Locate platelets.
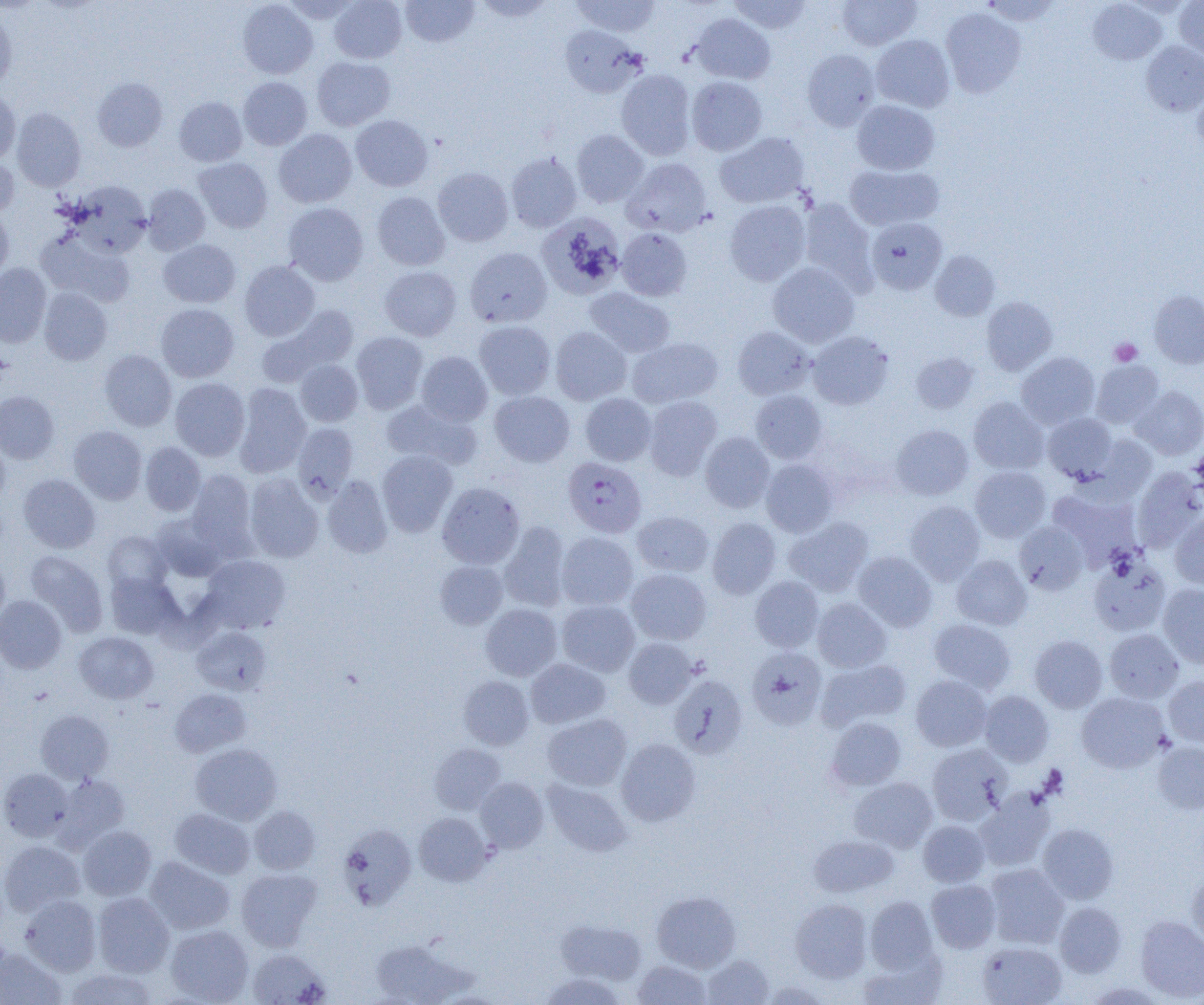

Approximate bounding boxes as [x1, y1, x2, y2] in pixels.
Platelets: [1109, 338, 1142, 365].

slide_level_diagnosis: Plasmodium falciparum
magnification: 1000x
plasmodium_falciparum_infected_red_blood_cell_locations: 'approximate bounding boxes as [x1, y1, x2, y2] in pixels: [563, 457, 646, 538]'
field_of_view: single
image_size: 1204×1005 pixels
modality: optical microscopy
preparation: thin blood film
uninfected_red_blood_cell_locations: 'approximate bounding boxes as [x1, y1, x2, y2] in pixels: [281, 0, 361, 23], [329, 0, 407, 63], [401, 0, 479, 47], [472, 0, 557, 22], [570, 0, 661, 37], [728, 0, 812, 34], [837, 0, 921, 50], [980, 0, 1062, 26], [1175, 0, 1204, 61], [238, 1, 317, 79], [1088, 1, 1166, 65], [0, 8, 17, 91], [941, 8, 1026, 98], [691, 14, 775, 84], [560, 25, 642, 97], [871, 35, 955, 112], [1141, 41, 1204, 115], [802, 49, 880, 131], [312, 56, 395, 130], [616, 69, 696, 159], [686, 76, 767, 156], [92, 77, 168, 151], [238, 77, 312, 150], [1193, 84, 1204, 155], [0, 92, 21, 164], [174, 97, 247, 166], [852, 99, 940, 175], [12, 107, 86, 192], [350, 115, 433, 191], [274, 129, 357, 208], [572, 130, 649, 207], [715, 132, 810, 208], [506, 151, 582, 232], [0, 154, 19, 219], [193, 157, 272, 233], [622, 158, 712, 237], [844, 164, 944, 232], [433, 167, 513, 246], [70, 181, 151, 256], [143, 184, 210, 255], [372, 192, 450, 270], [798, 198, 877, 293], [724, 200, 811, 286], [283, 203, 368, 285], [0, 207, 14, 281], [536, 212, 625, 299], [867, 217, 947, 295], [617, 228, 692, 301], [36, 230, 135, 308], [158, 239, 240, 308], [465, 247, 552, 328], [930, 250, 1000, 321], [239, 260, 320, 341], [768, 262, 859, 348], [0, 264, 51, 347], [380, 266, 462, 341], [39, 287, 112, 365], [585, 287, 675, 358], [1149, 290, 1204, 369], [981, 297, 1057, 376], [155, 304, 239, 382], [258, 305, 358, 386], [474, 320, 556, 400], [733, 326, 814, 399], [550, 327, 632, 405], [808, 331, 894, 409], [351, 332, 428, 414], [627, 337, 724, 408], [99, 350, 177, 430], [416, 351, 492, 426], [911, 352, 980, 414], [1016, 352, 1100, 429], [295, 359, 363, 427], [1091, 360, 1165, 428], [170, 378, 250, 460], [233, 383, 311, 478], [1132, 386, 1204, 459], [750, 390, 827, 463], [0, 391, 59, 463], [489, 391, 575, 467], [580, 393, 656, 466], [644, 396, 722, 480], [968, 397, 1049, 474], [380, 398, 481, 470], [1042, 413, 1117, 482], [293, 423, 358, 500], [891, 424, 973, 500], [69, 426, 147, 504], [700, 432, 774, 512], [0, 436, 10, 506], [1088, 436, 1157, 502], [140, 441, 205, 516], [377, 450, 457, 536], [760, 459, 839, 537], [970, 466, 1051, 542], [1132, 468, 1204, 551], [186, 469, 257, 554], [18, 473, 100, 552], [245, 473, 323, 563], [322, 475, 392, 558], [437, 482, 525, 569], [1047, 487, 1141, 570], [905, 501, 985, 584], [633, 511, 714, 576], [152, 513, 227, 581], [1170, 513, 1204, 589], [784, 516, 873, 596], [707, 517, 780, 599], [499, 521, 571, 612], [1014, 522, 1088, 595], [103, 531, 171, 594], [556, 532, 638, 610], [25, 550, 108, 637], [853, 551, 937, 632], [0, 552, 10, 628], [201, 555, 291, 632], [951, 555, 1032, 630], [1088, 557, 1171, 636], [435, 561, 508, 629], [626, 568, 711, 645], [106, 572, 182, 639], [750, 576, 824, 652], [1158, 584, 1204, 668], [0, 595, 67, 674], [812, 598, 892, 672], [557, 600, 640, 676], [481, 604, 562, 681], [929, 618, 1016, 694], [191, 626, 271, 694], [1104, 629, 1183, 703], [75, 632, 158, 703], [1029, 635, 1108, 713], [623, 637, 698, 708], [747, 647, 827, 730], [526, 658, 610, 728], [817, 659, 911, 732], [668, 674, 748, 759], [458, 675, 533, 749], [911, 675, 993, 752], [1164, 676, 1204, 746], [170, 688, 252, 757], [980, 691, 1054, 766], [1076, 692, 1169, 773], [35, 710, 114, 784], [542, 713, 631, 791], [826, 717, 906, 791], [616, 738, 701, 826], [1152, 742, 1204, 813], [190, 743, 282, 824], [429, 743, 505, 814], [927, 744, 1012, 825], [0, 768, 74, 841], [53, 773, 130, 851], [475, 777, 548, 853], [849, 777, 937, 852], [542, 779, 632, 857], [975, 789, 1055, 871], [249, 805, 320, 874], [170, 808, 255, 879], [414, 813, 492, 886], [918, 820, 989, 887], [1038, 823, 1119, 904], [338, 825, 417, 910], [78, 826, 157, 900], [808, 834, 899, 897], [0, 841, 85, 916], [144, 856, 234, 935], [984, 864, 1069, 949], [236, 868, 322, 951], [1187, 872, 1204, 952], [926, 879, 1001, 953], [652, 891, 741, 972], [92, 892, 174, 977], [20, 895, 101, 976], [865, 896, 937, 972], [790, 899, 872, 982], [1055, 902, 1127, 977], [1135, 916, 1204, 1002], [556, 919, 646, 986], [166, 925, 254, 1004], [368, 938, 472, 1005], [977, 941, 1066, 1004], [0, 948, 66, 1005], [247, 948, 330, 1005], [858, 949, 945, 1005], [702, 954, 774, 1005], [633, 960, 711, 1004], [63, 968, 159, 1004], [539, 973, 626, 1005], [1083, 981, 1166, 1005]'